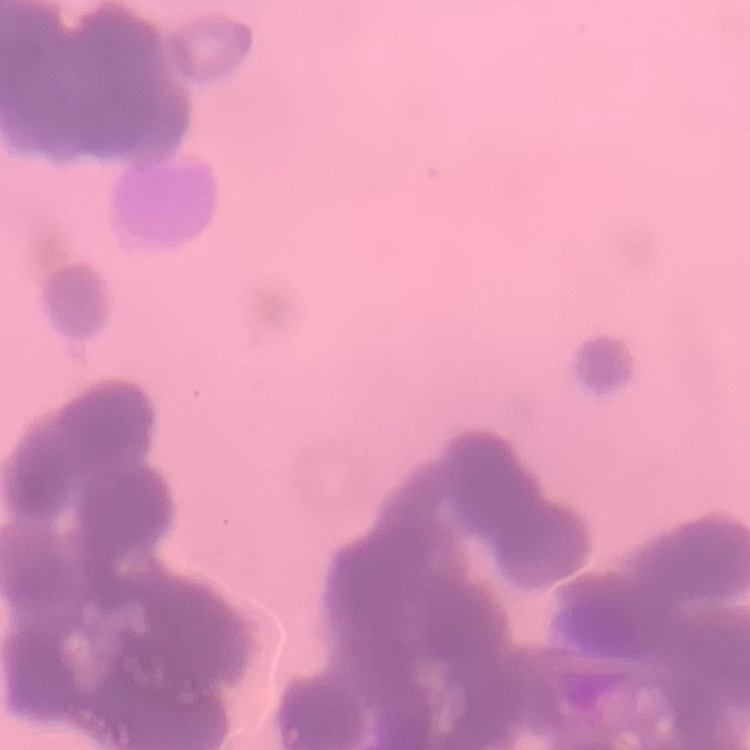
Summary:
  - Red blood cell morphology: rouleaux formation
  - Preparation: thin blood film
  - Stain: Field's or Giemsa
  - Image type: square crop of a larger photomicrograph